Report the malaria status of this cell.
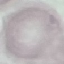

It is uninfected.

stain = Giemsa
capture = smartphone through the microscope eyepiece
preparation = thin blood film
image type = automatically extracted cell patch, resized to 64 × 64 pixels